Report the malaria status of this cell.
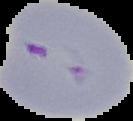
Parasitized.

{
  "preparation": "thin blood smear",
  "image_size": "133×121 pixels",
  "image_type": "segmented cell region on a black background"
}